Outline each blood parasite and name the species.
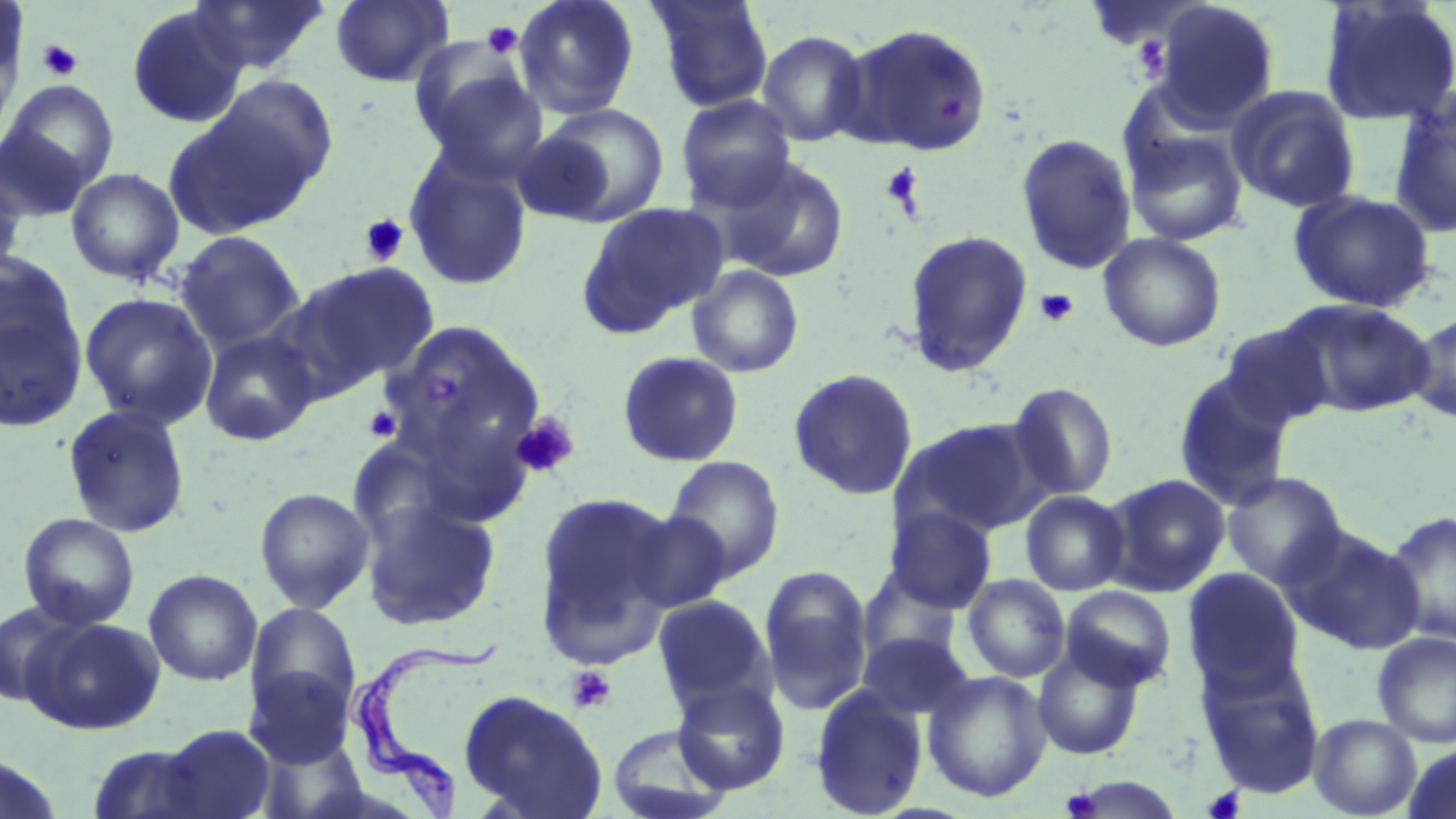

Approximate bounding boxes as (x1, y1, x2, y2) in pixels.
Trypanosoma brucei: (345, 638, 495, 818).
No Plasmodium falciparum, Plasmodium ovale, Plasmodium malariae, Plasmodium vivax, or Babesia divergens observed.

slide-level diagnosis = Trypanosoma brucei
magnification = 1000x
preparation = thin blood film
stain = May-Grünwald-Giemsa
field of view = one of a larger specimen
platelet locations = approximate bounding boxes as (x1, y1, x2, y2) in pixels: (481, 21, 523, 59), (1131, 37, 1171, 80), (36, 39, 84, 81), (936, 92, 966, 119), (881, 162, 925, 214), (359, 214, 409, 265), (1034, 288, 1079, 328), (363, 404, 402, 442), (509, 413, 579, 479), (566, 666, 617, 714), (1202, 786, 1245, 819), (1060, 788, 1101, 818)
image size = 1456×819 pixels
modality = optical microscopy
uninfected red blood cell locations = approximate bounding boxes as (x1, y1, x2, y2) in pixels: (186, 0, 332, 76), (330, 0, 454, 87), (513, 0, 640, 119), (647, 0, 774, 112), (155, 1, 322, 152), (1151, 1, 1280, 128), (1319, 1, 1456, 126), (126, 5, 248, 129), (0, 7, 27, 131), (839, 23, 992, 155), (756, 30, 871, 147), (414, 64, 549, 184), (179, 78, 338, 227), (3, 80, 119, 193), (1226, 85, 1361, 213), (1388, 88, 1456, 239), (675, 94, 797, 211), (533, 103, 670, 226), (0, 124, 91, 222), (1125, 129, 1248, 246), (1016, 133, 1137, 274), (402, 148, 534, 292), (716, 157, 850, 282), (0, 167, 28, 279), (66, 167, 185, 285), (1288, 189, 1437, 314), (577, 202, 728, 335), (904, 229, 1034, 377), (174, 230, 305, 353), (1098, 232, 1227, 352), (290, 260, 439, 392), (686, 265, 804, 377), (0, 272, 88, 434), (79, 292, 218, 430), (1278, 299, 1435, 418), (1406, 310, 1456, 423), (384, 319, 544, 471), (1218, 322, 1336, 430), (198, 330, 319, 446), (617, 351, 744, 467), (788, 368, 919, 500), (1172, 370, 1295, 510), (1006, 382, 1119, 501), (61, 403, 191, 538), (891, 417, 1048, 539), (664, 456, 785, 583), (1222, 471, 1349, 589), (1102, 474, 1231, 597), (255, 487, 375, 613), (1020, 490, 1131, 596), (533, 491, 681, 664), (360, 497, 501, 631), (884, 506, 997, 614), (1384, 509, 1456, 647), (624, 510, 734, 612), (18, 513, 140, 630), (1281, 525, 1427, 655), (759, 566, 874, 716), (1182, 568, 1304, 694), (144, 569, 262, 686), (962, 574, 1071, 683), (1060, 585, 1177, 690), (652, 594, 774, 713), (0, 599, 89, 709), (245, 603, 362, 724), (23, 616, 165, 735), (857, 631, 976, 722), (1372, 631, 1456, 748), (1033, 643, 1146, 761), (1195, 652, 1325, 797), (244, 666, 356, 767), (923, 670, 1052, 803), (672, 678, 791, 794), (809, 683, 928, 818), (458, 689, 608, 819), (1309, 713, 1422, 818), (606, 723, 733, 819), (155, 724, 277, 818), (86, 742, 216, 819), (1403, 743, 1456, 819), (0, 754, 67, 819), (1067, 775, 1174, 817)